Report the malaria status of this cell.
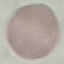

Uninfected.

capture = smartphone through the microscope eyepiece
preparation = thin blood film
image type = cell patch, automatically extracted from a larger field of view and resized to 64 × 64 pixels
stain = Giemsa